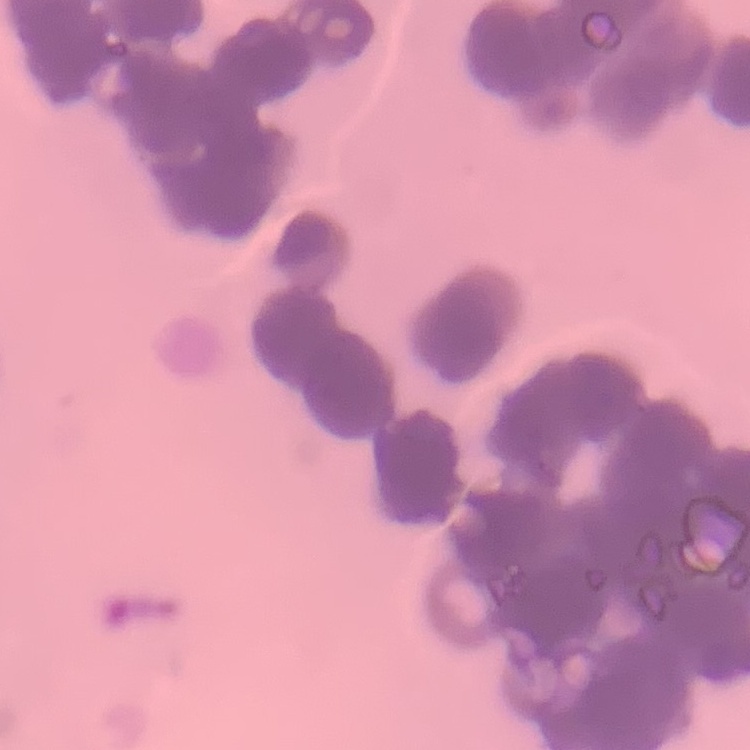
Summary:
  - Red blood cell morphology: rouleaux formation
  - Preparation: thin blood film
  - Stain: Field's or Giemsa
  - Image type: square crop of a larger photomicrograph